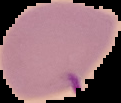

preparation = thin blood smear
image size = 121×103 pixels
malaria status = uninfected
image type = segmented cell region on a black background